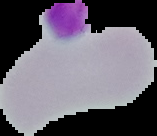
Summary:
  - Malaria status: uninfected
  - Preparation: thin blood smear
  - Image size: 157×136 pixels
  - Image type: segmented cell region with the area outside set to black